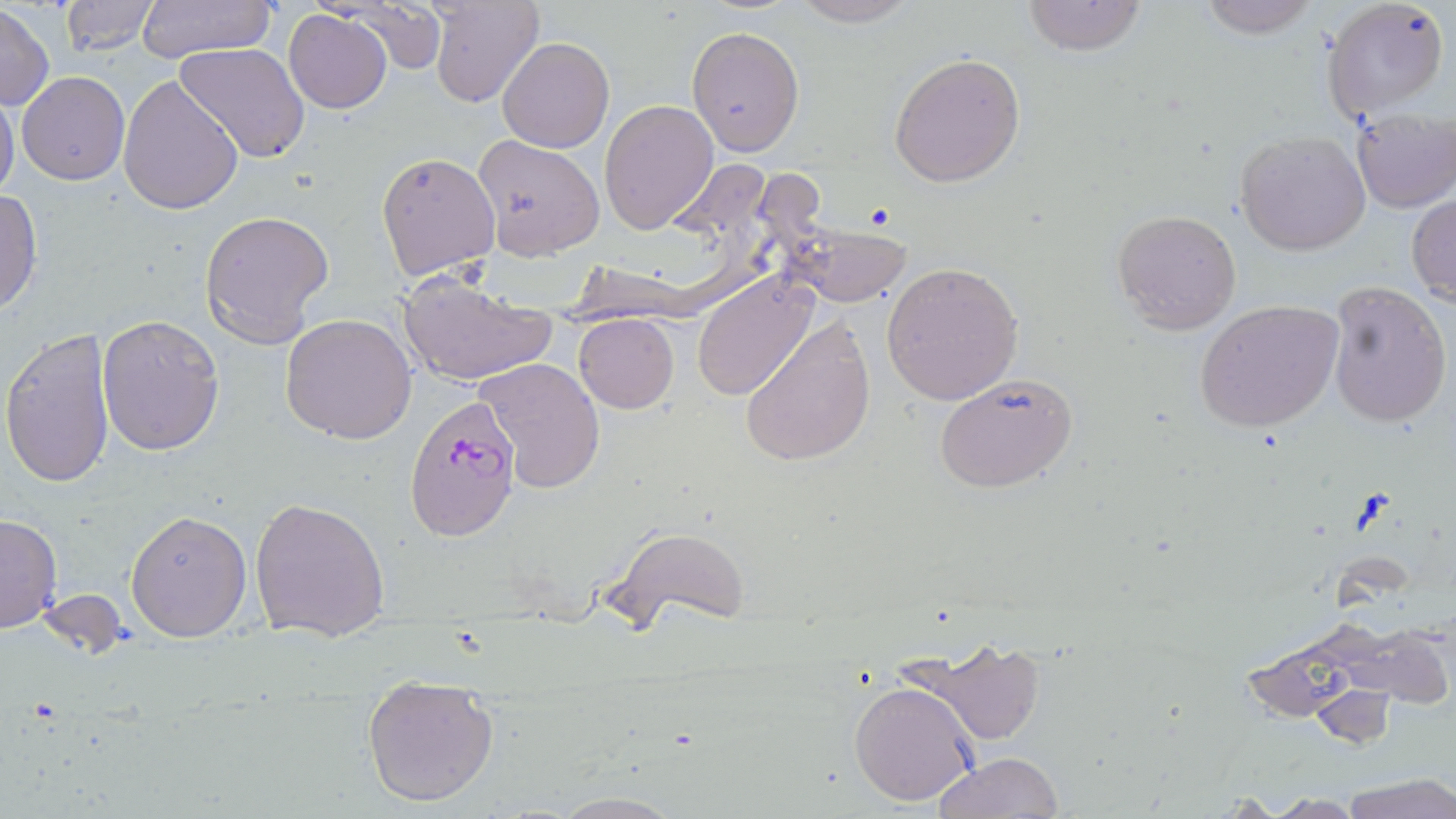
Summary:
  - Coordinate format: approximate bounding boxes as (x1,y1)-(x2,y2) corner pairs in pixels
  - Plasmodium falciparum-infected red blood cell locations: (404,395)-(522,541)
  - Uninfected red blood cell locations: (61,0)-(156,56), (136,0)-(276,65), (347,0)-(448,75), (430,0)-(542,107), (786,0)-(921,26), (1022,0)-(1148,55), (1197,0)-(1321,40), (1322,0)-(1449,120), (0,4)-(53,110), (283,8)-(392,113), (686,25)-(805,157), (497,37)-(614,153), (174,43)-(309,166), (888,53)-(1027,188), (18,72)-(130,185), (117,74)-(244,216), (0,93)-(20,204), (600,99)-(718,233), (1351,109)-(1456,212), (1234,130)-(1372,257), (472,133)-(606,259), (376,150)-(501,281), (0,188)-(42,316), (1407,193)-(1456,305), (200,209)-(334,345), (1111,209)-(1242,334), (782,222)-(913,309), (882,262)-(1024,405), (395,271)-(557,387), (692,273)-(817,400), (1326,280)-(1452,430), (1196,300)-(1344,434), (97,312)-(225,456), (282,312)-(417,445), (574,313)-(679,413), (738,316)-(876,468), (1,327)-(117,488), (474,356)-(607,493), (933,372)-(1080,493), (250,495)-(391,641), (126,510)-(251,643), (0,514)-(62,634), (608,525)-(746,631), (903,635)-(1049,746), (360,677)-(501,807), (849,680)-(980,807), (1311,684)-(1395,747), (935,751)-(1061,818), (1342,775)-(1456,819), (541,792)-(692,819), (1209,793)-(1292,816), (1268,794)-(1364,817)
  - Slide-level diagnosis: Plasmodium falciparum
  - Magnification: 1000x
  - Stain: May-Grünwald-Giemsa
  - Field of view: one of a larger specimen
  - Preparation: thin blood film
  - Modality: light microscopy
  - Image size: 1456×819 pixels